Report the malaria status of this cell.
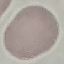
Uninfected.

Acquired by smartphone through the microscope eyepiece. Cell patch, automatically extracted from a larger field of view and resized to 64 × 64 pixels. Thin smear of blood. Giemsa stain.